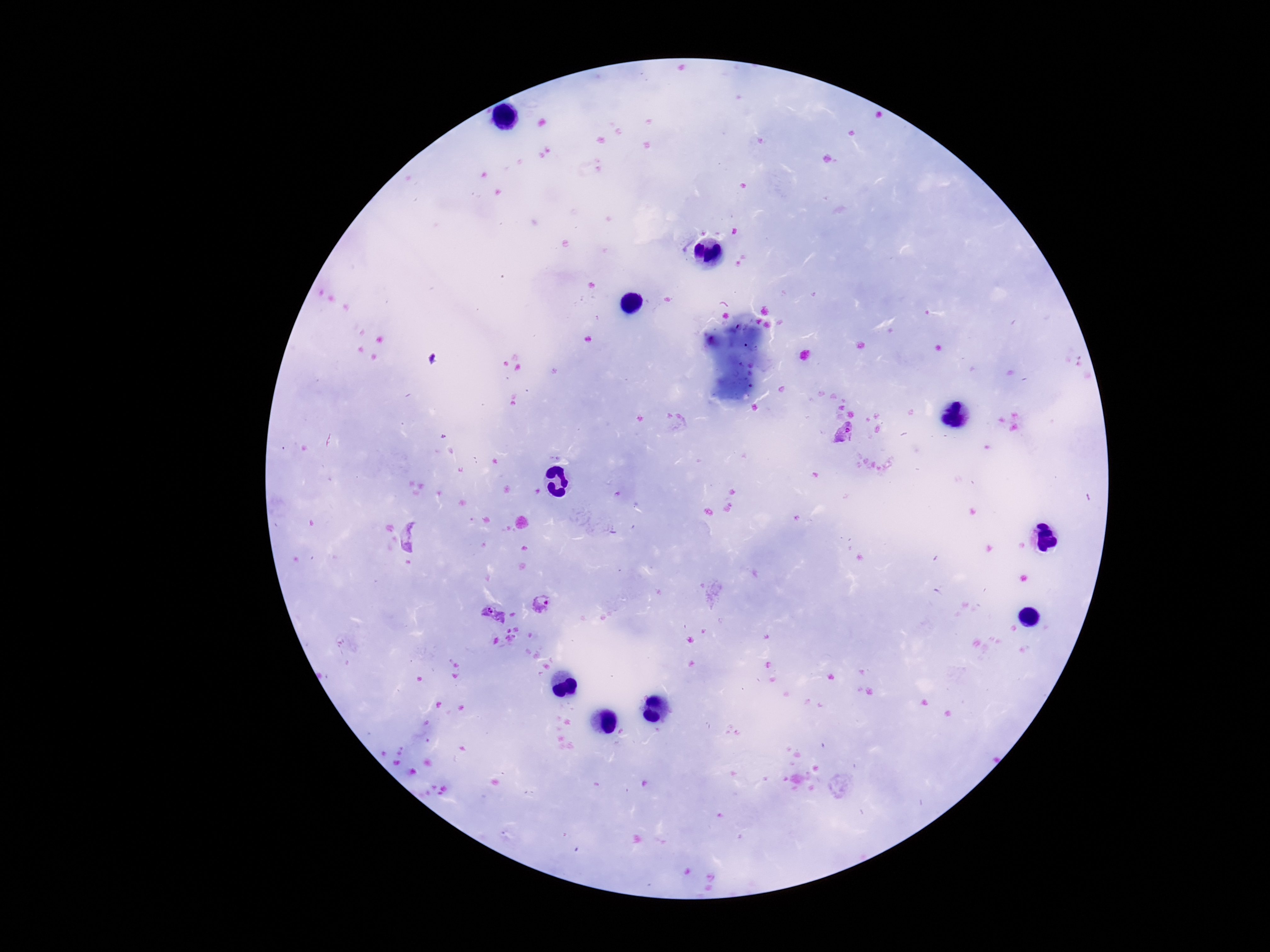
Approximate centers as (x, y) in pixels.
Summary:
  - Plasmodium parasite locations: (845, 434), (544, 604), (494, 615)
  - Patient malaria status: positive
  - Stain: Giemsa
  - Field of view: one from this slide
  - Capture: smartphone camera through the microscope eyepiece
  - Preparation: thick blood smear
  - Magnification: 100x
  - Image size: 1270×952 pixels